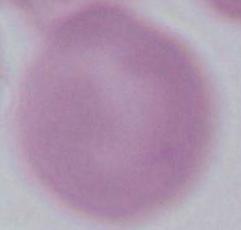
identification = red blood cell
magnification = 1000x
modality = micrograph